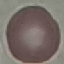

{
  "malaria_status": "uninfected",
  "stain": "Giemsa",
  "image_type": "cell patch, automatically extracted from a larger field of view and resized to 64 × 64 pixels",
  "capture": "smartphone camera at the microscope eyepiece",
  "preparation": "thin smear"
}